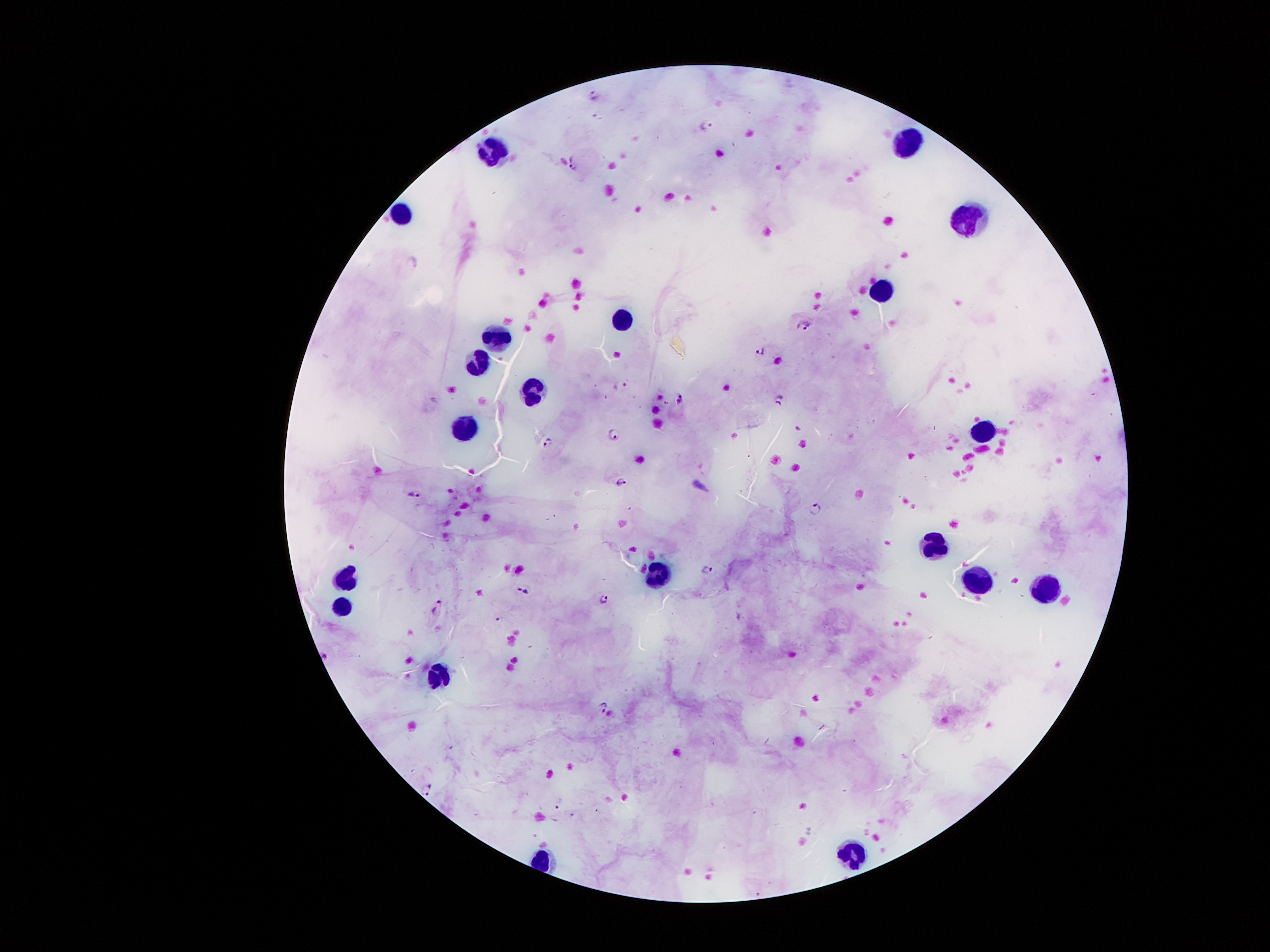

Approximate centers as (x, y) in pixels.
Summary:
  - Leukocyte locations: (907, 141), (492, 149), (401, 215), (970, 220), (882, 286), (618, 322), (495, 339), (475, 362), (534, 394), (462, 427), (981, 429), (930, 545), (657, 569), (344, 576), (972, 578), (1046, 585), (337, 603), (439, 674), (852, 852)
  - Malaria parasite locations: (593, 94), (706, 123), (573, 161), (412, 262), (803, 323), (761, 350), (622, 384), (778, 396), (678, 397), (614, 433), (548, 442), (1096, 457), (621, 480), (413, 493), (815, 506), (706, 569), (526, 589), (604, 597), (439, 607), (326, 654), (604, 706), (429, 785)
  - Preparation: thick blood film
  - Patient malaria status: infected with Plasmodium falciparum
  - Image size: 1270×952 pixels
  - Stain: Giemsa
  - Field of view: one from this slide
  - Capture: smartphone through the microscope eyepiece
  - Magnification: 100x